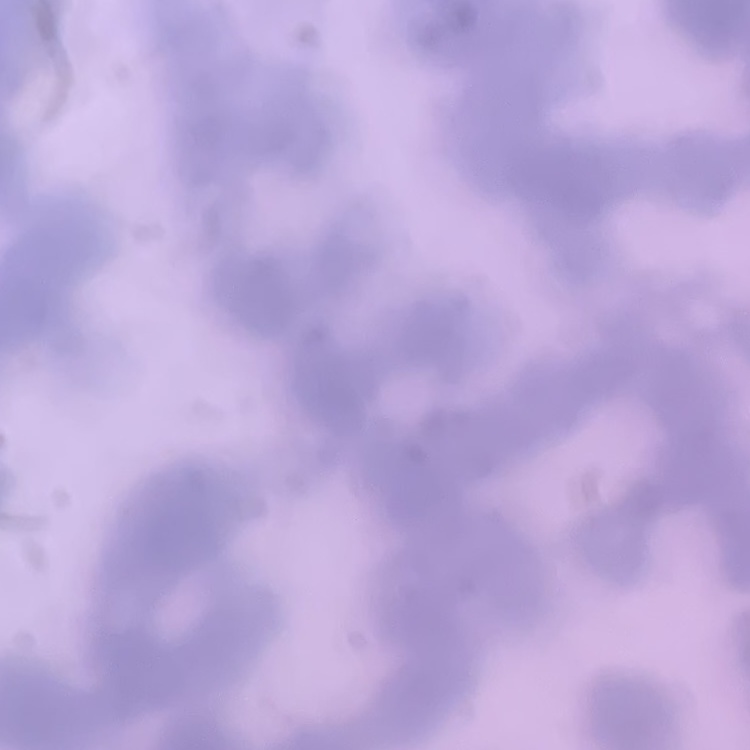

The erythrocytes show rouleaux formation. Square crop of a larger photomicrograph. Thin peripheral smear. Field's or Giemsa stain.